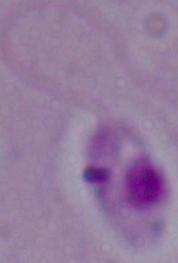
Summary:
  - Modality: micrograph
  - Identification: Leishmania
  - Magnification: 1000x